State which parasite is depicted.
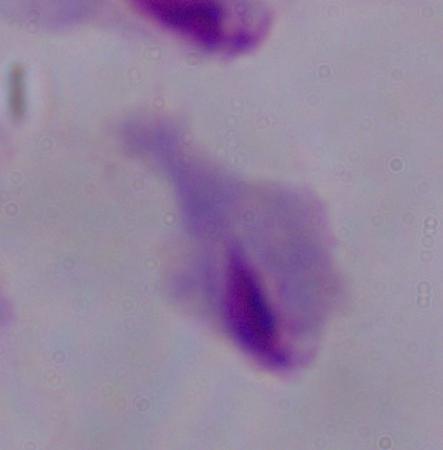
This is a trichomonad.

magnification: 1000x
modality: micrograph